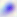

identification: Toxoplasma gondii
modality: micrograph
magnification: 400x